Describe the morphology of the erythrocytes.
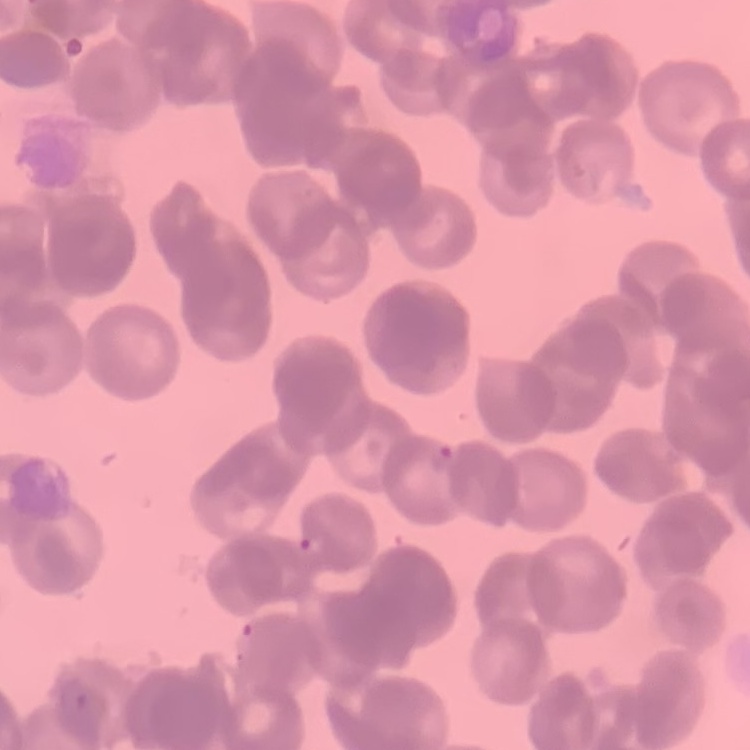

Rouleaux formation.

image type = one tile cut from a larger photomicrograph
stain = Field's or Giemsa
preparation = thin blood smear